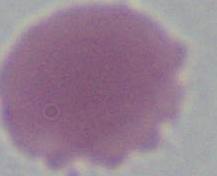
magnification = 1000x
identification = red blood cell
modality = micrograph